Comment on the morphology of the erythrocytes.
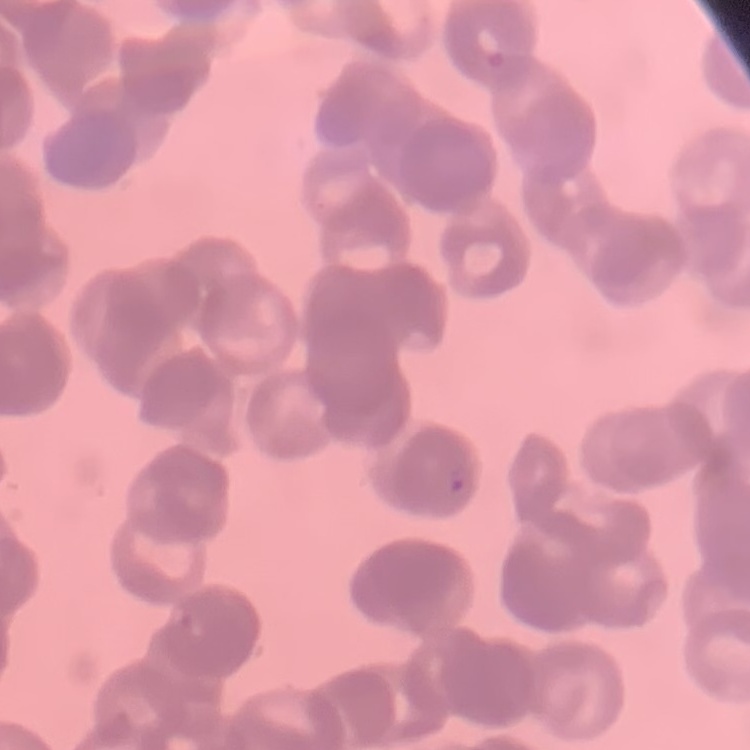
They show rouleaux formation.

Summary:
  - Image type: one tile cut from a larger photomicrograph
  - Stain: Field's or Giemsa
  - Preparation: thin blood film